Outline each blood parasite and name the species.
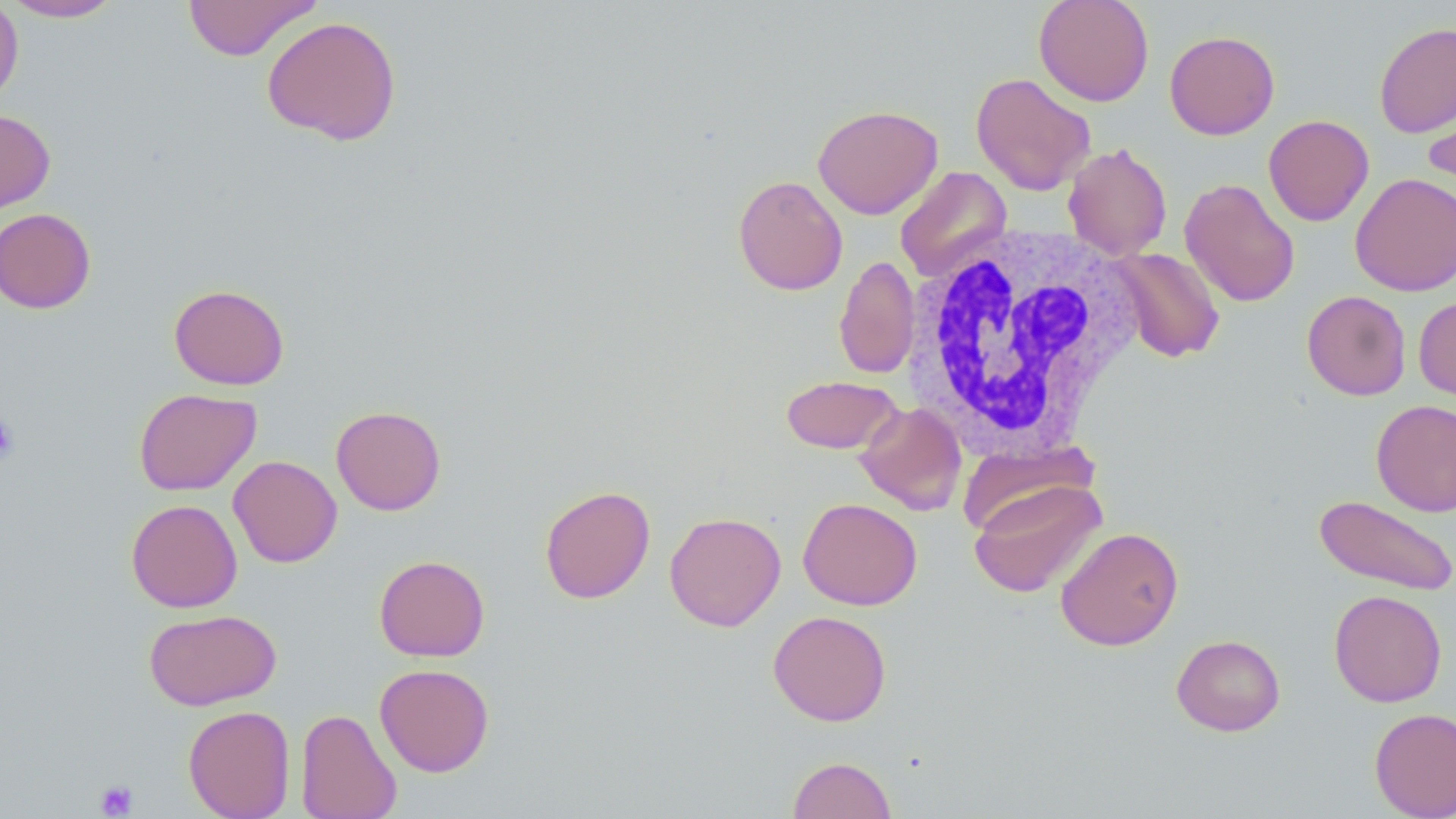
No blood parasites observed.

slide-level diagnosis = negative for blood parasites
field of view = one of a larger specimen
image size = 1456×819 pixels
modality = optical microscopy
preparation = thin blood film
uninfected red blood cell locations = approximate bounding boxes as [x1, y1, x2, y2] in pixels: [181, 0, 320, 61], [1033, 0, 1155, 106], [0, 1, 24, 106], [1, 1, 123, 22], [261, 15, 402, 145], [1374, 21, 1456, 139], [1164, 30, 1280, 140], [970, 72, 1096, 195], [1422, 89, 1456, 205], [813, 104, 943, 219], [0, 109, 56, 213], [1263, 114, 1374, 226], [1063, 143, 1173, 260], [895, 166, 1012, 282], [1350, 172, 1456, 296], [733, 175, 848, 296], [1180, 178, 1301, 307], [0, 207, 96, 314], [1106, 247, 1226, 363], [834, 255, 920, 379], [169, 283, 290, 390], [1301, 290, 1412, 401], [1414, 295, 1456, 408], [781, 375, 903, 454], [133, 388, 261, 496], [1371, 399, 1456, 516], [855, 402, 966, 515], [331, 405, 446, 515], [228, 455, 342, 568], [968, 479, 1106, 598], [539, 485, 655, 604], [1314, 495, 1455, 595], [798, 497, 922, 610], [126, 499, 243, 612], [664, 511, 787, 632], [1055, 526, 1184, 651], [373, 555, 490, 661], [1328, 589, 1447, 707], [144, 608, 282, 710], [767, 610, 892, 726], [1171, 634, 1285, 736], [374, 664, 495, 777], [182, 705, 296, 819], [295, 707, 402, 819], [1369, 707, 1456, 819], [787, 756, 898, 818]
white blood cell locations = approximate bounding boxes as [x1, y1, x2, y2] in pixels: [903, 223, 1145, 457]
magnification = 1000x
stain = May-Grünwald-Giemsa
platelet locations = approximate bounding boxes as [x1, y1, x2, y2] in pixels: [0, 410, 20, 467], [94, 780, 138, 818]